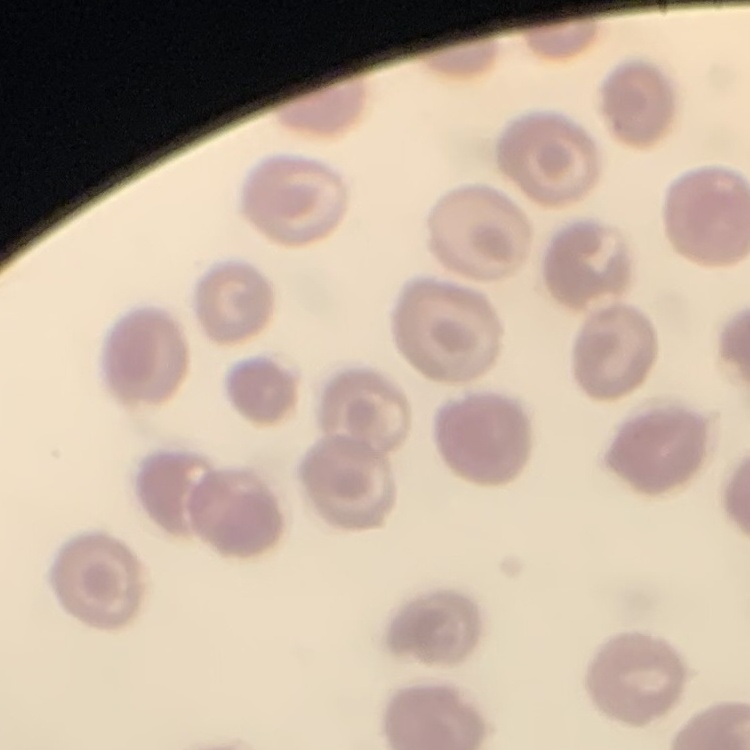
red blood cell morphology = no rouleaux formation
stain = Field's or Giemsa
preparation = thin blood film
image type = one tile cut from a larger photomicrograph